Identify the parasite.
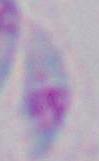

Toxoplasma gondii.

{
  "magnification": "1000x",
  "modality": "photomicrograph"
}